State which parasite is depicted.
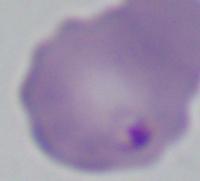

Babesia.

1000x magnification. Photomicrograph.